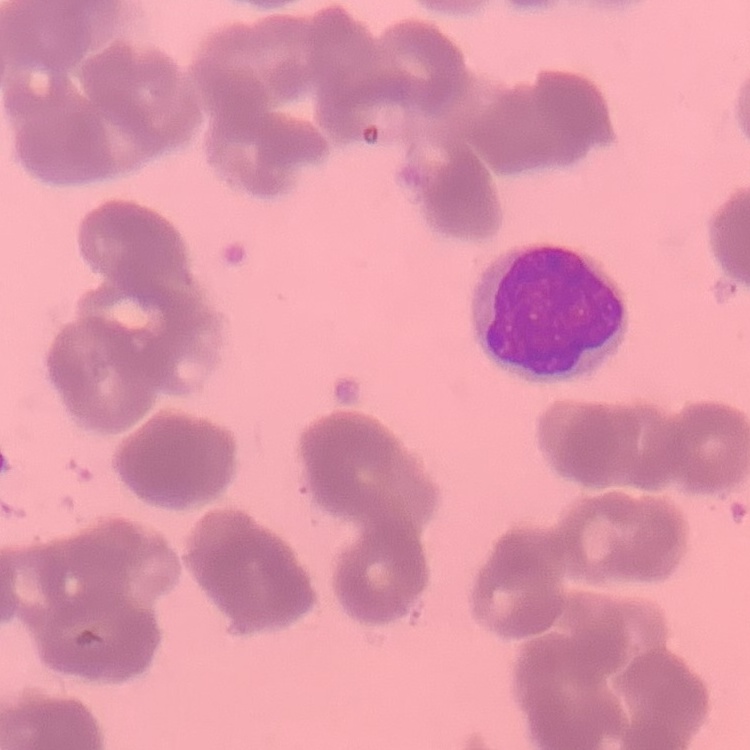

{
  "erythrocyte_morphology": "rouleaux formation",
  "image_type": "square crop of a larger photomicrograph",
  "stain": "Field's or Giemsa",
  "preparation": "thin blood smear"
}